Assess this cell for malaria.
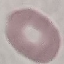
It is uninfected.

Summary:
  - Preparation: thin smear
  - Stain: Giemsa
  - Capture: smartphone through the microscope eyepiece
  - Image type: cell patch, automatically extracted from a larger field of view and resized to 64 × 64 pixels